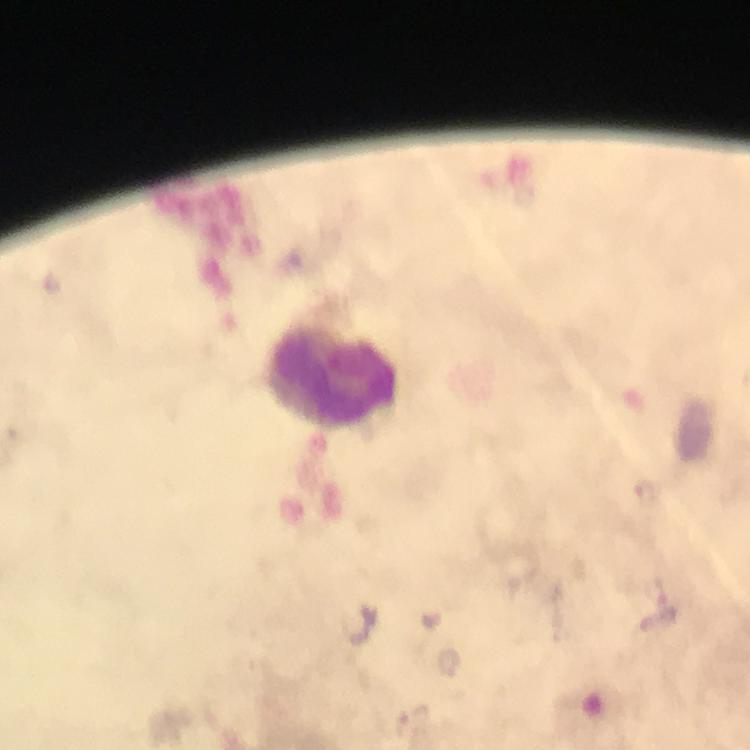

Approximate object centers, in pixels from the top-left corner. Leukocyte locations: (x=332, y=380). Immersion oil was used. From a malaria diagnostic workup. Photographed through the microscope with a smartphone camera. A crop from one field of view. Giemsa stain. Plasmodium parasites: none seen. Image is 750×750 pixels. Thick smear. 100x magnification.